Assess this cell for malaria.
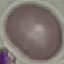

Uninfected.

Giemsa-stained preparation. Automatically extracted cell patch, resized to 64 × 64 pixels. Photographed with a smartphone camera at the microscope eyepiece. Thin blood smear.